Point out each malaria parasite.
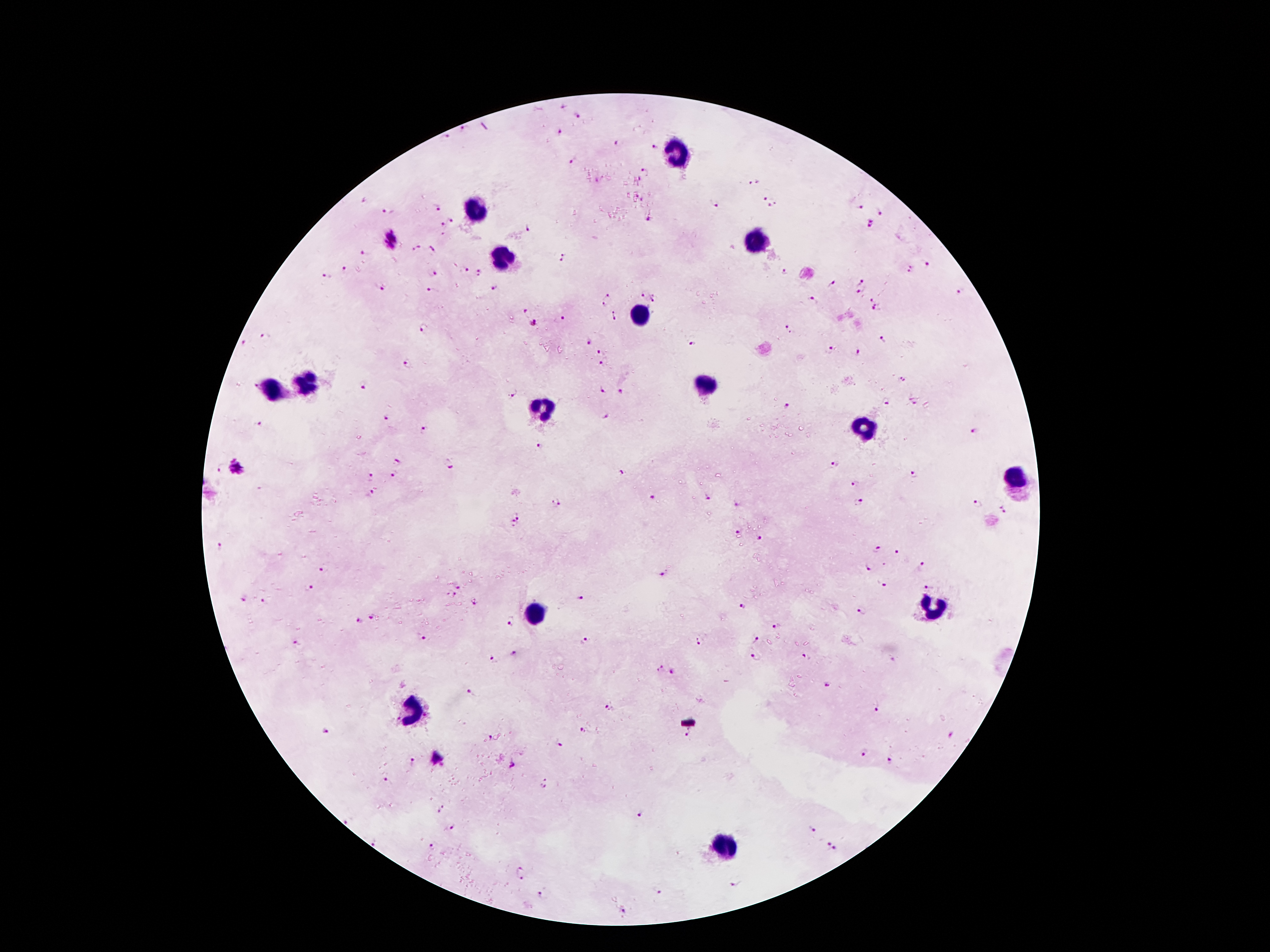

Approximate centers as {x, y} in pixels.
Malaria parasites: {561, 105}, {578, 115}, {463, 129}, {559, 132}, {444, 136}, {617, 144}, {654, 146}, {575, 160}, {644, 171}, {754, 181}, {766, 198}, {363, 200}, {776, 202}, {715, 203}, {770, 204}, {859, 205}, {438, 207}, {389, 211}, {881, 212}, {648, 218}, {452, 221}, {441, 224}, {870, 224}, {529, 227}, {391, 240}, {417, 247}, {430, 249}, {365, 253}, {565, 256}, {926, 264}, {345, 268}, {464, 269}, {909, 269}, {784, 270}, {480, 273}, {432, 274}, {327, 276}, {833, 281}, {863, 281}, {380, 287}, {495, 288}, {430, 289}, {858, 291}, {960, 291}, {641, 293}, {608, 295}, {656, 298}, {870, 298}, {812, 299}, {604, 305}, {526, 308}, {876, 308}, {614, 314}, {559, 319}, {532, 324}, {787, 327}, {424, 328}, {265, 336}, {883, 339}, {587, 343}, {692, 344}, {244, 345}, {830, 348}, {601, 352}, {858, 353}, {601, 364}, {407, 366}, {902, 378}, {365, 385}, {603, 390}, {513, 392}, {621, 392}, {911, 399}, {884, 401}, {786, 406}, {604, 415}, {386, 419}, {259, 424}, {424, 429}, {973, 430}, {540, 447}, {395, 460}, {450, 463}, {833, 464}, {236, 468}, {621, 471}, {395, 474}, {913, 474}, {370, 477}, {855, 484}, {369, 494}, {650, 496}, {708, 496}, {556, 502}, {859, 502}, {977, 503}, {737, 504}, {1004, 509}, {520, 515}, {512, 524}, {737, 531}, {760, 539}, {220, 547}, {877, 550}, {896, 553}, {923, 566}, {868, 568}, {322, 569}, {663, 574}, {883, 584}, {928, 585}, {457, 586}, {309, 588}, {452, 595}, {243, 598}, {580, 598}, {262, 600}, {473, 602}, {741, 607}, {862, 610}, {373, 618}, {510, 620}, {358, 622}, {776, 625}, {421, 638}, {755, 639}, {585, 640}, {698, 642}, {297, 643}, {516, 654}, {754, 656}, {806, 657}, {493, 660}, {658, 667}, {672, 672}, {828, 686}, {470, 693}, {609, 707}, {876, 708}, {326, 730}, {581, 730}, {951, 734}, {687, 735}, {489, 737}, {557, 744}, {863, 753}, {436, 758}, {412, 761}, {891, 761}, {512, 766}, {386, 780}, {545, 783}, {440, 810}, {637, 814}, {347, 819}, {452, 828}, {812, 830}, {374, 842}, {430, 845}, {831, 846}, {521, 872}, {736, 884}, {658, 891}, {540, 894}, {624, 913}.

capture: smartphone camera through the microscope eyepiece
field_of_view: single
magnification: 100x
leukocyte_locations: 'approximate centers as {x, y} in pixels: {675, 148}, {477, 206}, {757, 242}, {502, 254}, {639, 314}, {304, 382}, {704, 385}, {271, 387}, {541, 408}, {864, 428}, {1014, 477}, {930, 606}, {535, 612}, {411, 711}, {724, 846}'
stain: Giemsa
patient_malaria_status: positive for Plasmodium falciparum
image_size: 1270×952 pixels
preparation: thick peripheral-blood smear